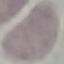
Summary:
  - Result: negative for malaria parasites
  - Stain: Giemsa
  - Preparation: thin blood smear
  - Capture: smartphone through the microscope eyepiece
  - Image type: automatically extracted cell patch, resized to 64 × 64 pixels